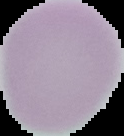

Summary:
  - Malaria status: uninfected
  - Image size: 124×136 pixels
  - Preparation: thin blood smear
  - Image type: segmented cell region on a black background